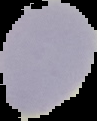
Summary:
  - Preparation: thin blood film
  - Image type: segmented cell region on a black background
  - Result: no Plasmodium parasites detected
  - Image size: 97×121 pixels